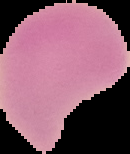
Image is 130×154 pixels. The area outside the segmented cell region is set to black. Malaria status: uninfected. From a thin blood film.